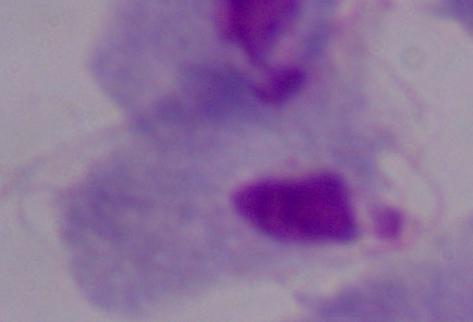

Summary:
  - Identification: trichomonad
  - Modality: photomicrograph
  - Magnification: 1000x